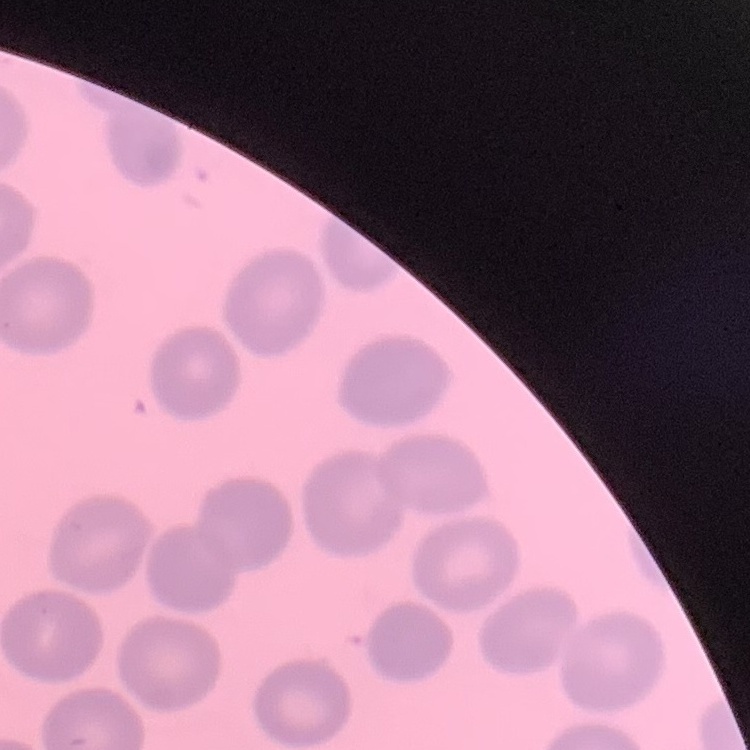

The red blood cells exhibit no rouleaux formation. Thin blood smear. Square crop of a larger photomicrograph. Field's or Giemsa stain.